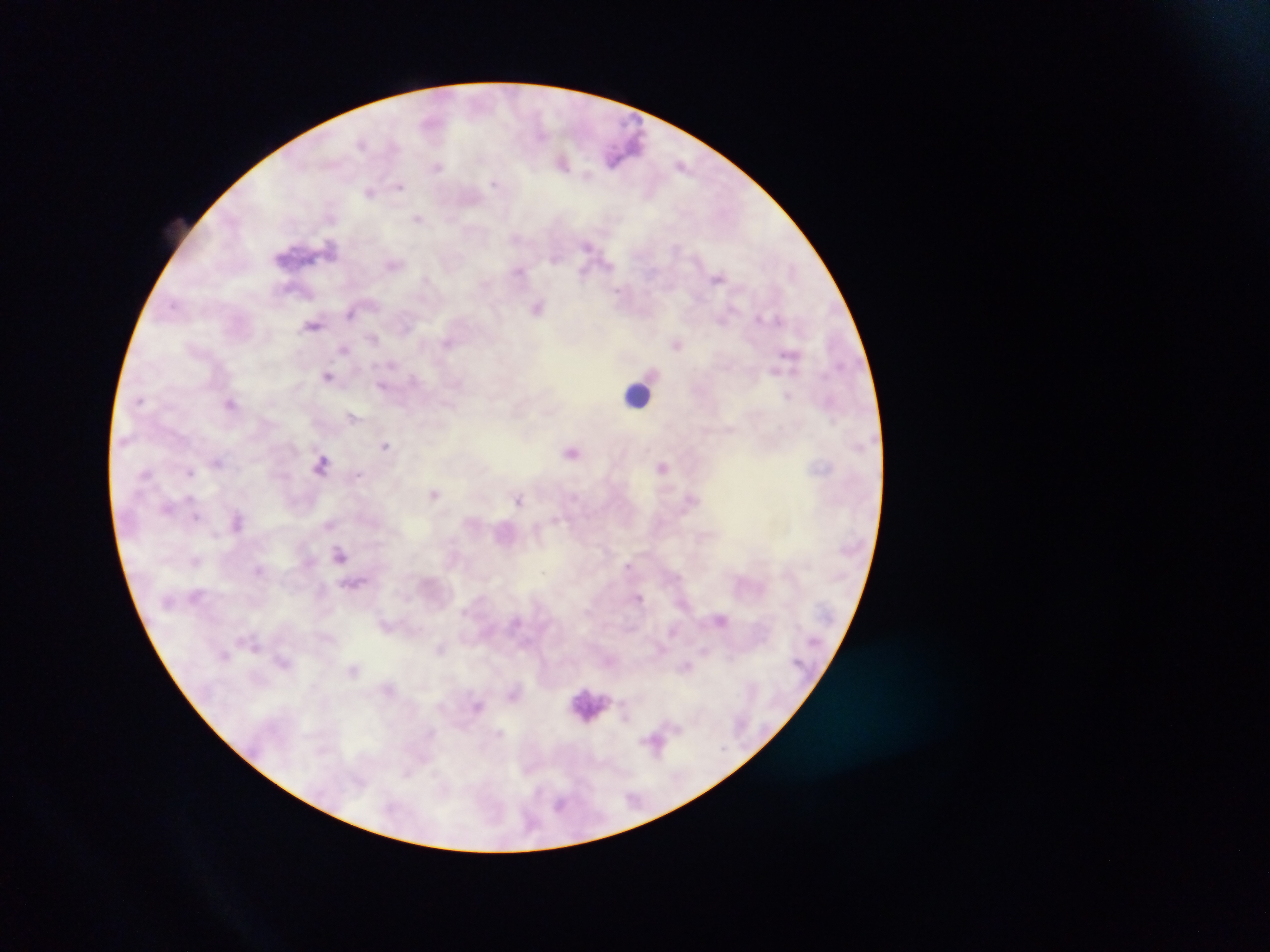

Approximate centers as x y in pixels. Leukocyte locations: 636 394. Plasmodium parasite locations: 563 162; 683 162; 437 167; 495 184; 400 186; 370 192; 419 218; 587 246; 331 247; 519 272; 717 277; 426 280; 538 307; 351 314; 766 317; 311 328; 374 337; 446 342; 676 344; 344 350; 789 353; 391 365; 776 371; 327 375; 383 386; 788 396; 230 402; 518 410; 548 411; 355 415; 730 431; 385 446; 572 452; 218 462; 322 465; 662 466; 190 471; 434 494; 689 495; 519 500; 197 516; 556 520; 562 520; 329 525; 341 555; 195 562; 628 565; 256 570; 640 597; 721 621; 673 631; 243 637; 440 648; 707 649; 732 657; 687 666; 625 715; 650 740. Single field of view. Mobile-phone photograph taken through the microscope. Thick blood smear. Sample from Ghana. Image is 1270×952 pixels.